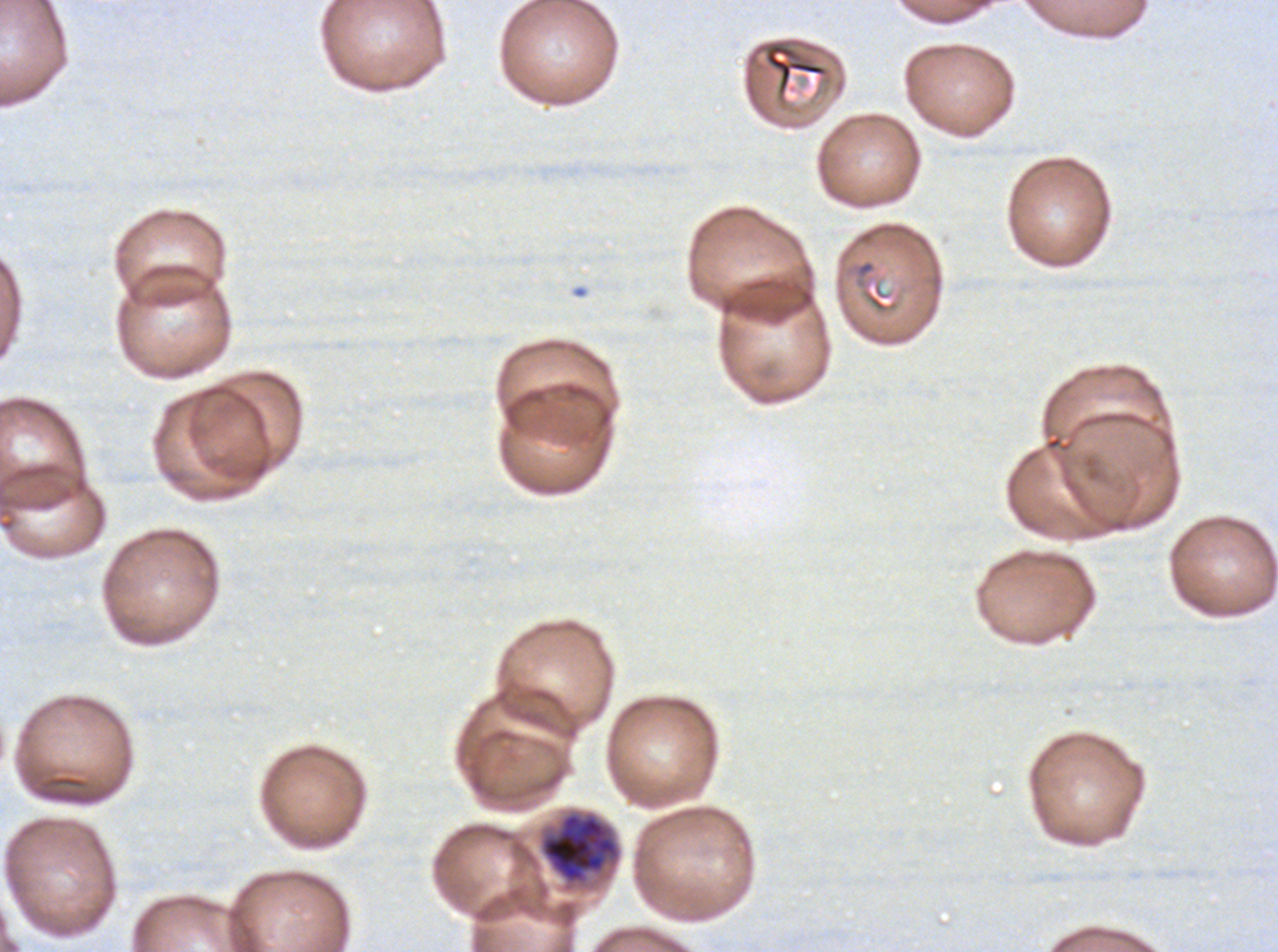

Approximate bounding boxes as {x1, y1, x2, y2} in pixels. Debris locations: {765, 44, 826, 91}, {850, 258, 900, 314}. Late schizont locations: {541, 812, 619, 884}. Image is 1278×952 pixels. Giemsa stain. A sub-image separated from a larger composite. Thin blood smear. Plasmodium falciparum cultured ex vivo for 24 to 48 hours, from a patient in The Gambia.